Locate every parasitized red blood cell.
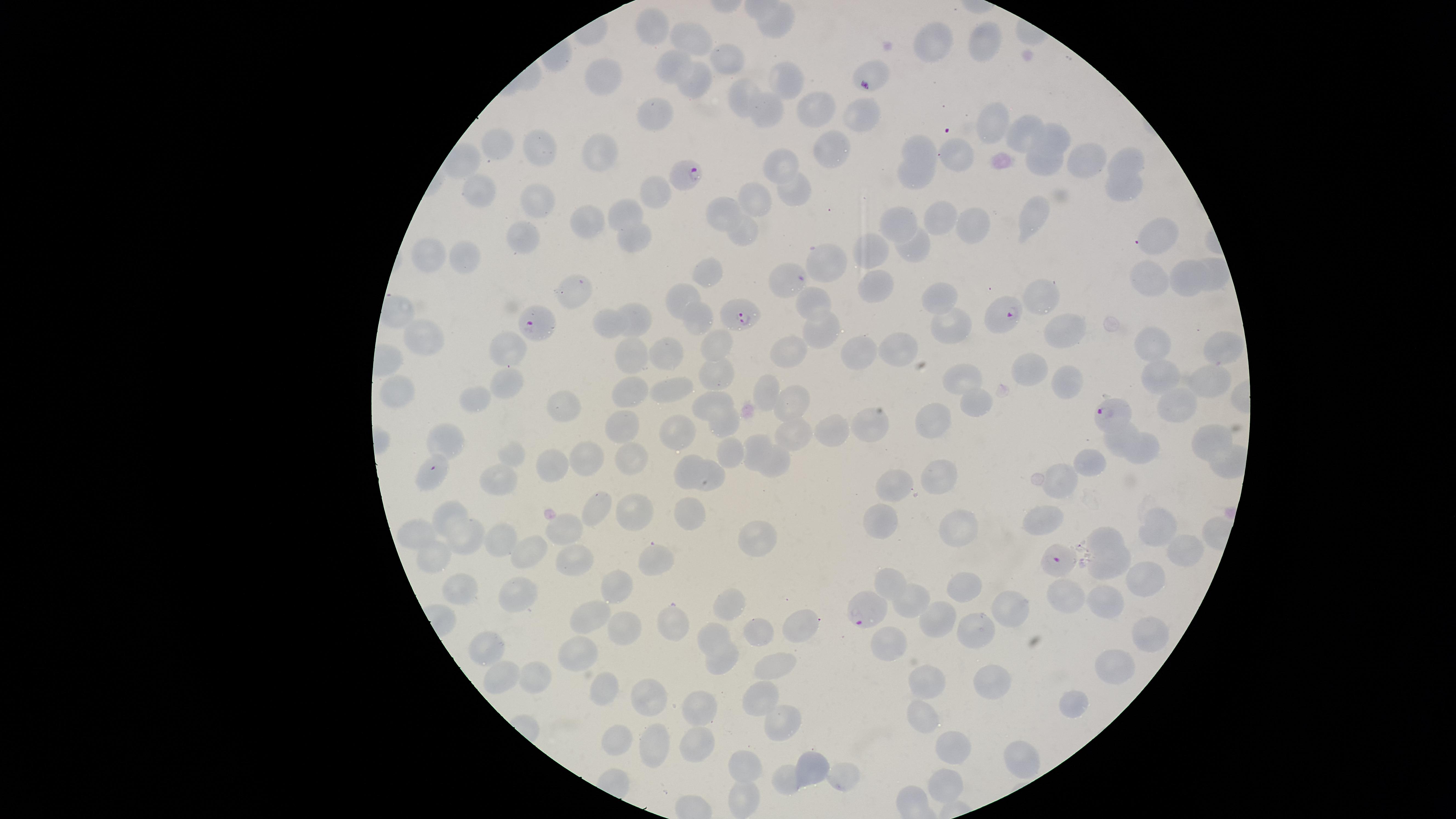

Approximate marker points as {x, y} in pixels.
Parasitized red blood cells: {866, 85}, {694, 172}, {1006, 312}, {738, 314}, {533, 324}, {1109, 413}, {1055, 559}, {863, 612}.

Approximate marker points as {x, y} in pixels. Uninfected red blood cells: {655, 21}, {777, 24}, {692, 37}, {986, 41}, {937, 43}, {671, 60}, {731, 60}, {605, 77}, {785, 77}, {688, 79}, {747, 98}, {823, 110}, {769, 111}, {655, 112}, {861, 112}, {989, 123}, {1023, 126}, {1055, 135}, {503, 143}, {920, 144}, {540, 146}, {601, 151}, {959, 151}, {831, 155}, {1084, 156}, {1130, 160}, {1045, 161}, {783, 162}, {915, 174}, {1124, 180}, {480, 181}, {654, 188}, {795, 189}, {755, 198}, {536, 200}, {728, 210}, {1035, 212}, {625, 214}, {946, 214}, {590, 219}, {906, 223}, {745, 229}, {977, 229}, {632, 235}, {1161, 235}, {524, 239}, {918, 243}, {880, 249}, {431, 252}, {467, 255}, {821, 262}, {710, 271}, {1217, 271}, {1152, 278}, {1192, 280}, {882, 282}, {784, 287}, {570, 292}, {686, 292}, {1041, 294}, {936, 295}, {814, 301}, {631, 318}, {698, 318}, {953, 320}, {612, 326}, {818, 329}, {1073, 331}, {423, 340}, {722, 342}, {899, 346}, {506, 347}, {1154, 347}, {787, 353}, {861, 353}, {1222, 353}, {671, 354}, {635, 358}, {1028, 366}, {722, 373}, {1156, 374}, {967, 377}, {1072, 382}, {1214, 382}, {501, 383}, {773, 387}, {399, 388}, {678, 390}, {631, 393}, {797, 399}, {472, 401}, {1185, 401}, {717, 404}, {977, 405}, {565, 406}, {937, 411}, {626, 424}, {872, 427}, {836, 431}, {1207, 435}, {676, 436}, {796, 436}, {452, 440}, {1117, 440}, {757, 443}, {518, 451}, {587, 452}, {730, 454}, {1144, 454}, {628, 459}, {770, 463}, {551, 464}, {1091, 465}, {689, 469}, {941, 473}, {428, 475}, {712, 478}, {501, 480}, {897, 483}, {1063, 487}, {594, 506}, {450, 508}, {629, 508}, {685, 511}, {573, 520}, {882, 520}, {1043, 524}, {1157, 524}, {961, 528}, {468, 533}, {420, 534}, {1110, 535}, {510, 538}, {756, 540}, {530, 554}, {570, 554}, {1183, 555}, {432, 557}, {650, 558}, {1114, 570}, {1146, 576}, {896, 579}, {465, 586}, {961, 586}, {617, 587}, {1113, 594}, {911, 597}, {731, 601}, {1064, 601}, {518, 603}, {1012, 607}, {593, 612}, {673, 615}, {941, 615}, {800, 621}, {619, 625}, {761, 629}, {980, 631}, {719, 632}, {1149, 633}, {890, 641}, {490, 651}, {581, 651}, {722, 658}, {773, 666}, {1113, 668}, {509, 673}, {544, 676}, {990, 680}, {608, 682}, {929, 683}, {759, 697}, {645, 698}, {697, 705}, {1070, 706}, {923, 712}, {785, 717}, {619, 738}, {695, 743}, {956, 744}, {663, 748}, {1020, 755}, {811, 762}, {749, 764}, {843, 778}, {948, 779}, {788, 781}, {747, 800}. Species: Plasmodium falciparum. Thin blood smear. Giemsa-stained preparation. Photographed with a smartphone camera through the microscope eyepiece. Circular visible region. One field of view of the specimen. Image is 1456×819 pixels.